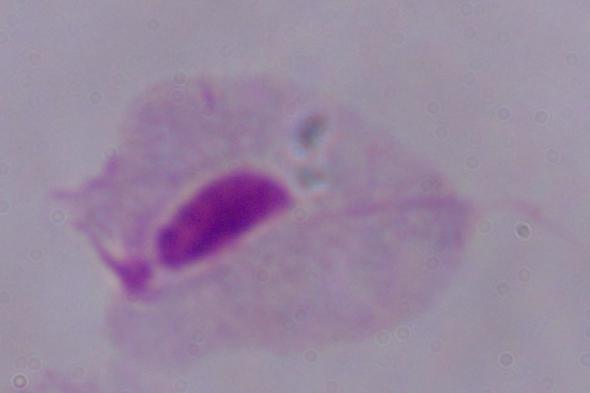
{
  "modality": "micrograph",
  "identification": "trichomonad",
  "magnification": "1000x"
}